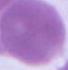

magnification: 1000x
modality: photomicrograph
identification: erythrocyte